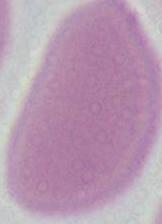 Captured at 1000x magnification. Photomicrograph. A red blood cell is seen.